Identify the parasite.
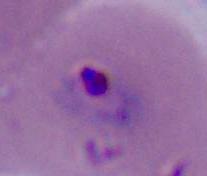

Plasmodium.

magnification = 400x or 1000x
modality = micrograph